Identify the blood parasite species.
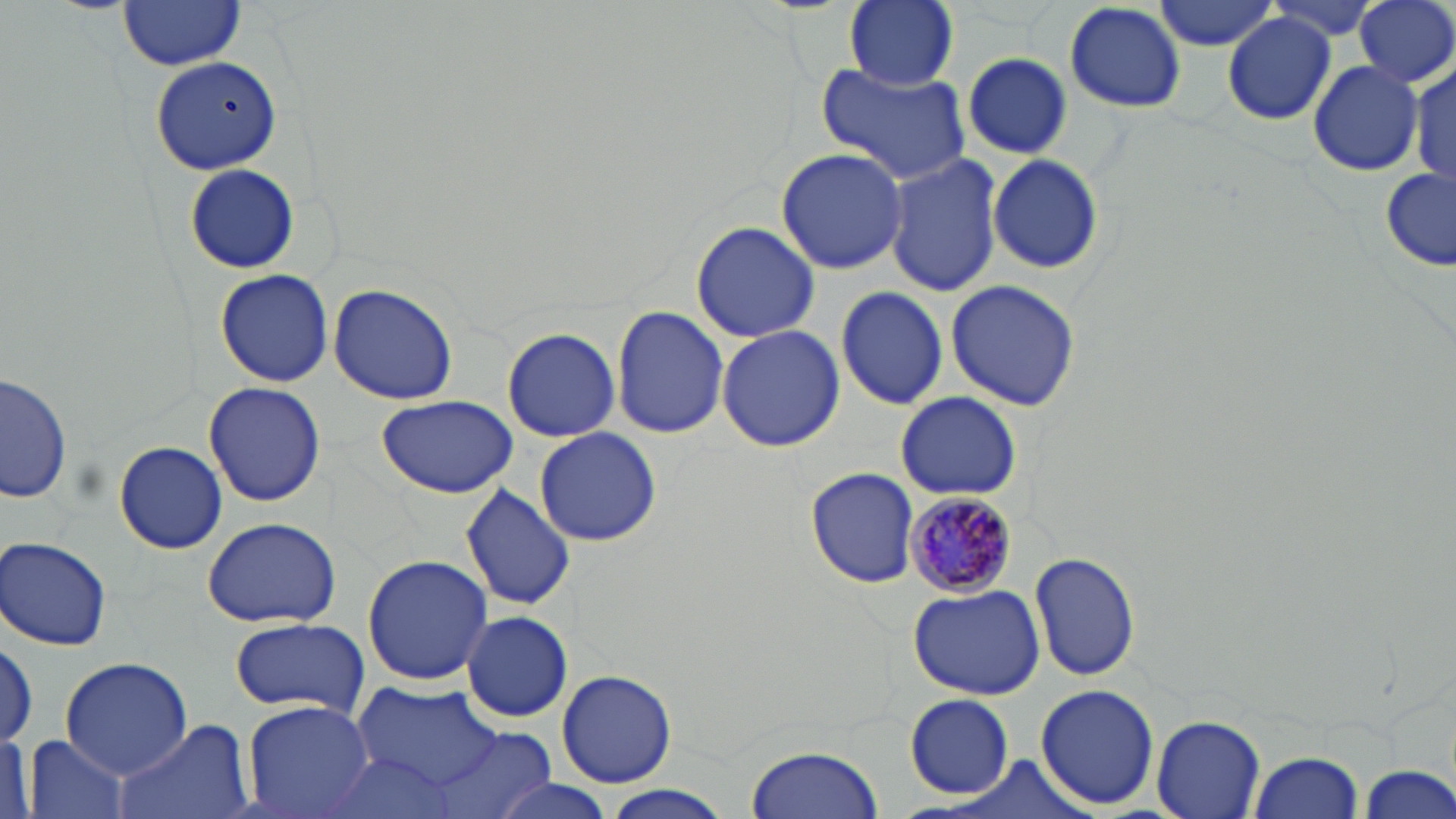

Plasmodium malariae.

preparation = thin blood film
field of view = single
image size = 1456×819 pixels
magnification = 1000x
stain = May-Grünwald-Giemsa
modality = light microscopy
uninfected red blood cell locations = approximate bounding boxes as (x1,y1)-(x2,y2) corner pairs in pixels: (845,0)-(958,90), (1061,0)-(1189,113), (1153,0)-(1283,51), (1262,0)-(1390,44), (1356,0)-(1456,89), (118,1)-(245,71), (1222,13)-(1339,126), (962,54)-(1075,161), (149,56)-(280,175), (814,62)-(971,185), (1309,63)-(1424,175), (1413,63)-(1453,189), (775,147)-(909,275), (883,153)-(1003,295), (987,154)-(1105,275), (184,163)-(300,274), (1380,166)-(1456,271), (690,220)-(819,344), (214,269)-(336,387), (946,279)-(1080,410), (330,283)-(458,405), (834,285)-(950,410), (611,306)-(730,438), (716,325)-(844,453), (502,327)-(621,442), (2,372)-(76,505), (203,382)-(327,505), (895,392)-(1022,500), (374,394)-(517,498), (535,427)-(661,546), (116,440)-(227,555), (805,467)-(917,588), (461,483)-(575,612), (201,516)-(341,629), (2,536)-(113,650), (1030,549)-(1141,683), (362,553)-(492,685), (906,583)-(1044,699), (460,609)-(573,722), (228,617)-(369,717), (59,657)-(191,776), (557,668)-(676,787), (1034,683)-(1160,812), (352,685)-(501,786), (906,694)-(1015,798), (243,700)-(374,819), (1151,714)-(1265,819), (109,719)-(252,819), (428,727)-(557,819), (0,731)-(32,819), (22,734)-(132,819), (747,744)-(882,819), (319,749)-(468,819), (1249,750)-(1363,818), (1354,762)-(1456,819), (483,780)-(626,819), (602,787)-(733,817)
Plasmodium malariae-infected red blood cell locations = approximate bounding boxes as (x1,y1)-(x2,y2) corner pairs in pixels: (906,490)-(1013,599)